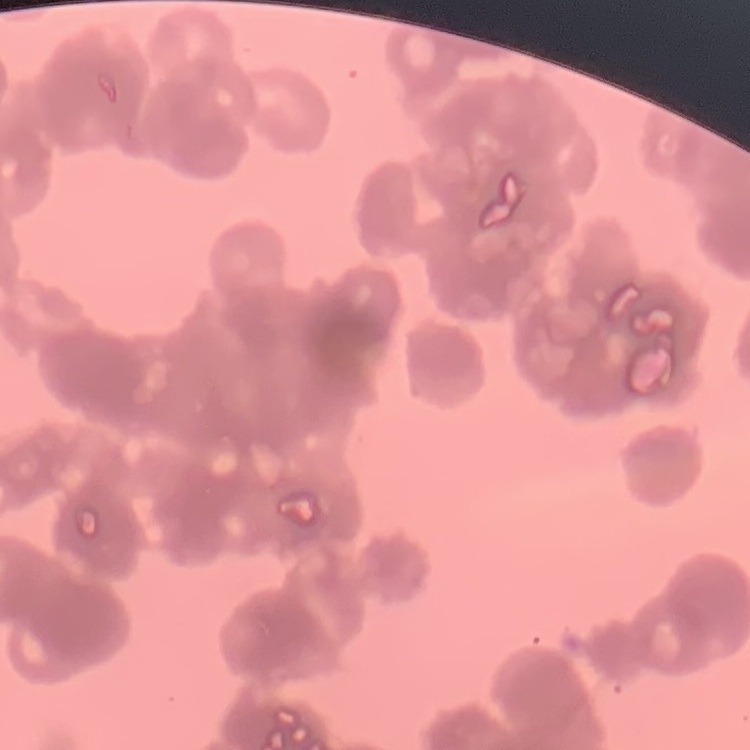

Summary:
  - Erythrocyte morphology: rouleaux formation
  - Image type: one tile cut from a larger photomicrograph
  - Stain: Field's or Giemsa
  - Preparation: thin blood film